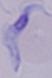
Photomicrograph. A trypanosome is shown. Captured at 1000x magnification.